Comment on the morphology of the red blood cells.
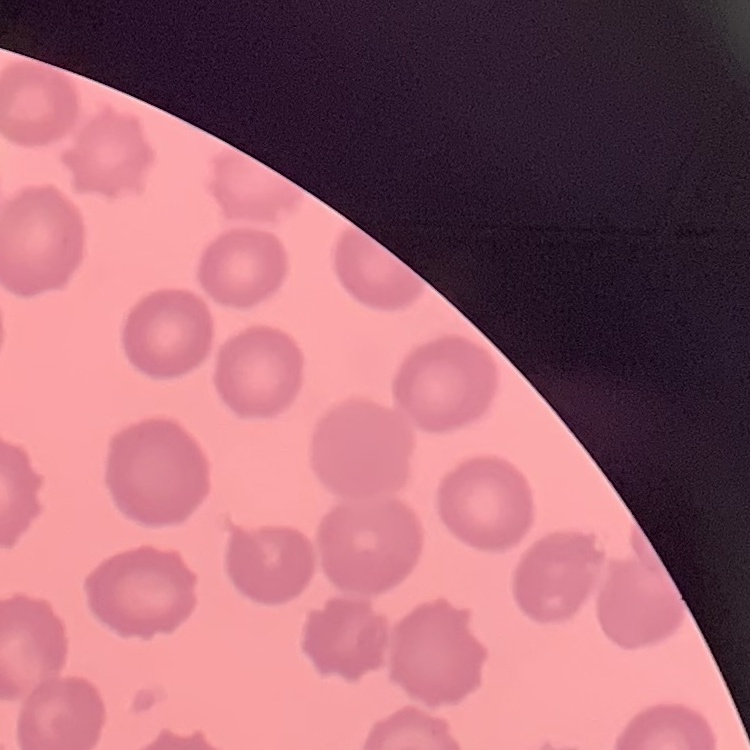
They show no rouleaux formation.

Square crop of a larger photomicrograph. Thin blood smear. Field's or Giemsa stain.